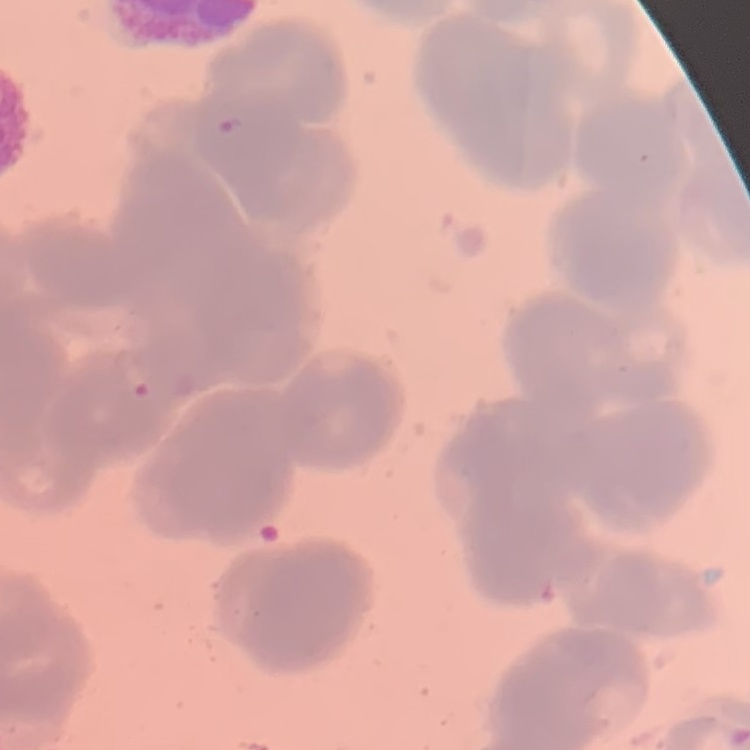

red blood cell morphology = rouleaux formation
stain = Field's or Giemsa
image type = one tile cut from a larger photomicrograph
preparation = thin blood film